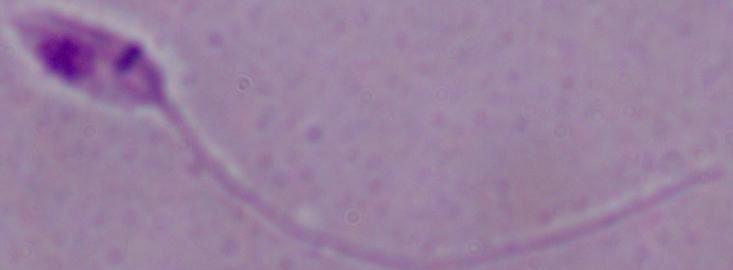 1000x magnification. A Leishmania parasite is seen. Micrograph.